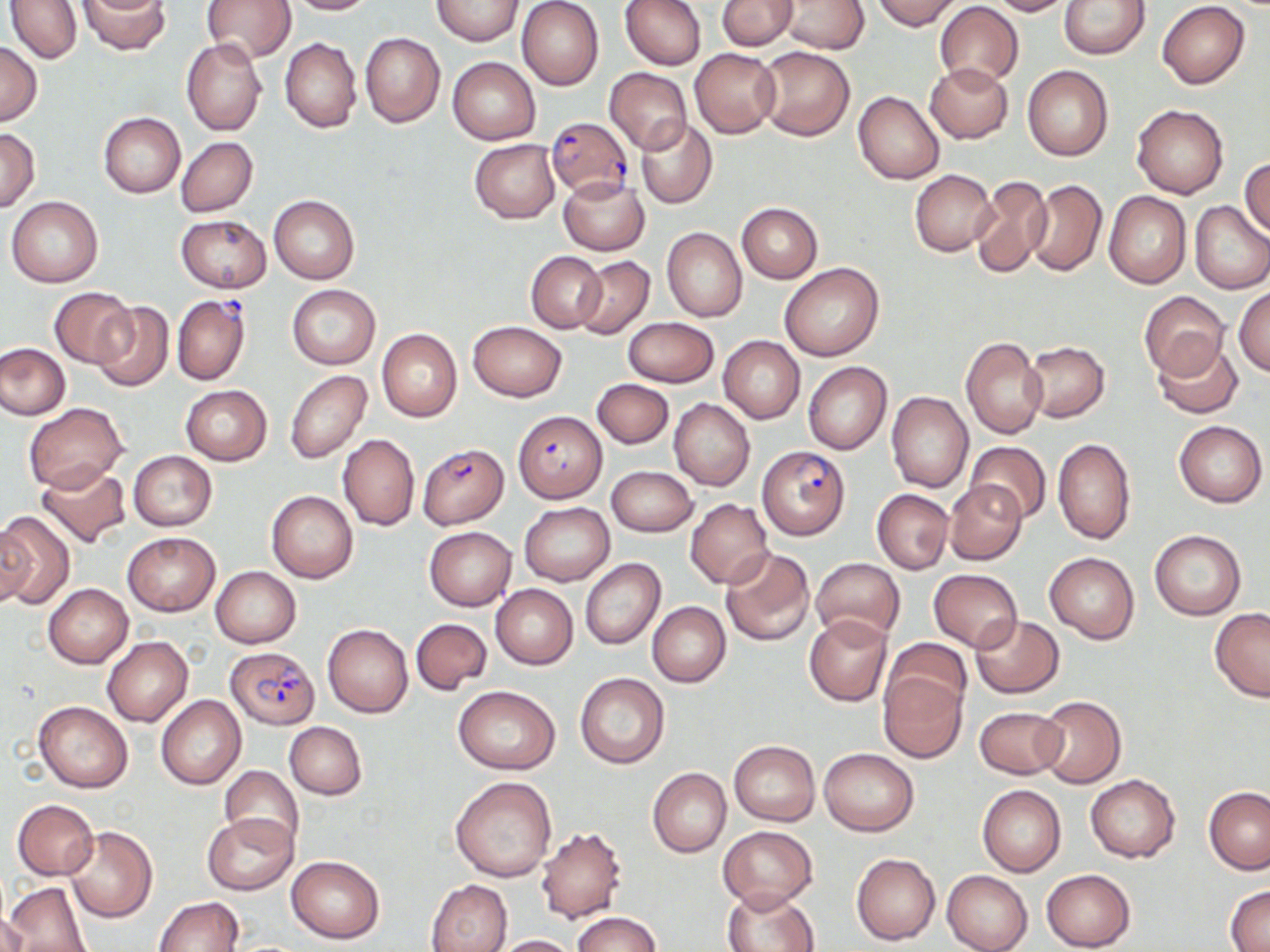
Summary:
  - Coordinate format: approximate bounding boxes as (x1,y1)-(x2,y2) corner pairs in pixels
  - Plasmodium falciparum-infected red blood cell locations: (546,117)-(633,199), (169,293)-(252,384), (513,410)-(607,503), (418,443)-(508,528), (758,446)-(850,540), (226,645)-(320,729)
  - Uninfected red blood cell locations: (5,0)-(83,64), (79,0)-(169,55), (201,0)-(296,63), (282,0)-(373,14), (432,0)-(524,44), (517,0)-(604,90), (619,0)-(705,71), (873,0)-(960,30), (985,0)-(1071,16), (1058,0)-(1149,58), (717,1)-(796,50), (776,1)-(868,53), (1157,1)-(1249,88), (935,2)-(1025,86), (360,32)-(445,128), (280,38)-(361,133), (182,39)-(267,136), (0,41)-(43,126), (754,46)-(855,140), (690,48)-(780,136), (448,56)-(541,145), (924,62)-(1013,143), (1023,65)-(1113,162), (605,68)-(692,153), (853,90)-(944,184), (1132,105)-(1228,199), (98,113)-(185,198), (637,118)-(717,208), (0,128)-(39,212), (176,136)-(257,216), (469,139)-(560,224), (1240,157)-(1269,237), (910,169)-(998,256), (969,175)-(1053,277), (559,177)-(649,255), (1023,179)-(1107,277), (1104,192)-(1191,288), (269,195)-(359,283), (7,196)-(104,287), (1191,201)-(1270,294), (737,203)-(822,283), (177,215)-(270,292), (662,228)-(746,321), (527,251)-(605,332), (574,255)-(654,339), (780,263)-(883,362), (288,284)-(380,369), (1234,286)-(1270,375), (50,287)-(135,367), (1139,291)-(1229,380), (91,302)-(173,391), (623,317)-(719,388), (467,321)-(567,401), (376,329)-(462,422), (718,335)-(805,423), (961,336)-(1048,439), (1022,340)-(1110,421), (1152,340)-(1242,418), (0,343)-(70,420), (803,362)-(892,455), (285,369)-(371,464), (593,379)-(673,449), (181,384)-(272,464), (886,391)-(973,492), (669,398)-(755,490), (23,402)-(127,491), (1173,421)-(1266,507), (338,434)-(419,530), (1051,438)-(1136,545), (966,440)-(1051,524), (128,450)-(217,531), (36,462)-(130,550), (607,466)-(697,536), (945,481)-(1027,564), (872,489)-(953,574), (267,491)-(358,583), (685,499)-(773,588), (519,502)-(615,586), (0,511)-(74,609), (0,519)-(35,608), (424,526)-(516,610), (1150,529)-(1246,621), (124,532)-(219,615), (720,547)-(816,648), (1044,552)-(1140,643), (580,558)-(665,650), (811,558)-(905,644), (211,566)-(300,648), (928,568)-(1022,650), (43,584)-(133,667), (490,584)-(578,668), (647,601)-(730,687), (1209,609)-(1270,702), (804,615)-(892,707), (969,615)-(1064,698), (410,617)-(491,695), (323,623)-(413,717), (102,636)-(192,726), (881,639)-(970,723), (878,670)-(967,761), (576,672)-(669,769), (454,685)-(561,773), (156,695)-(246,789), (1036,695)-(1126,788), (34,701)-(133,793), (975,705)-(1065,779), (285,722)-(367,799), (728,740)-(819,826), (819,748)-(919,834), (219,765)-(304,851), (648,768)-(730,857), (1085,774)-(1181,862), (451,776)-(557,882), (977,785)-(1066,877), (1203,786)-(1270,874), (12,799)-(98,880), (203,813)-(297,895), (717,825)-(818,912), (64,826)-(157,923), (534,826)-(626,923), (851,852)-(940,945), (286,855)-(385,944), (1041,868)-(1136,951), (942,870)-(1033,952), (426,879)-(513,952), (3,881)-(91,952), (1225,886)-(1270,951), (722,887)-(819,952), (154,897)-(243,951), (573,911)-(659,952), (0,912)-(28,951), (487,935)-(580,952)
  - Slide-level diagnosis: Plasmodium falciparum
  - Preparation: thin blood smear
  - Field of view: single
  - Stain: May-Grünwald-Giemsa
  - Image size: 1270×952 pixels
  - Magnification: 1000x
  - Modality: optical microscopy